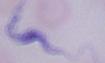

magnification = 1000x
modality = photomicrograph
identification = trypanosome